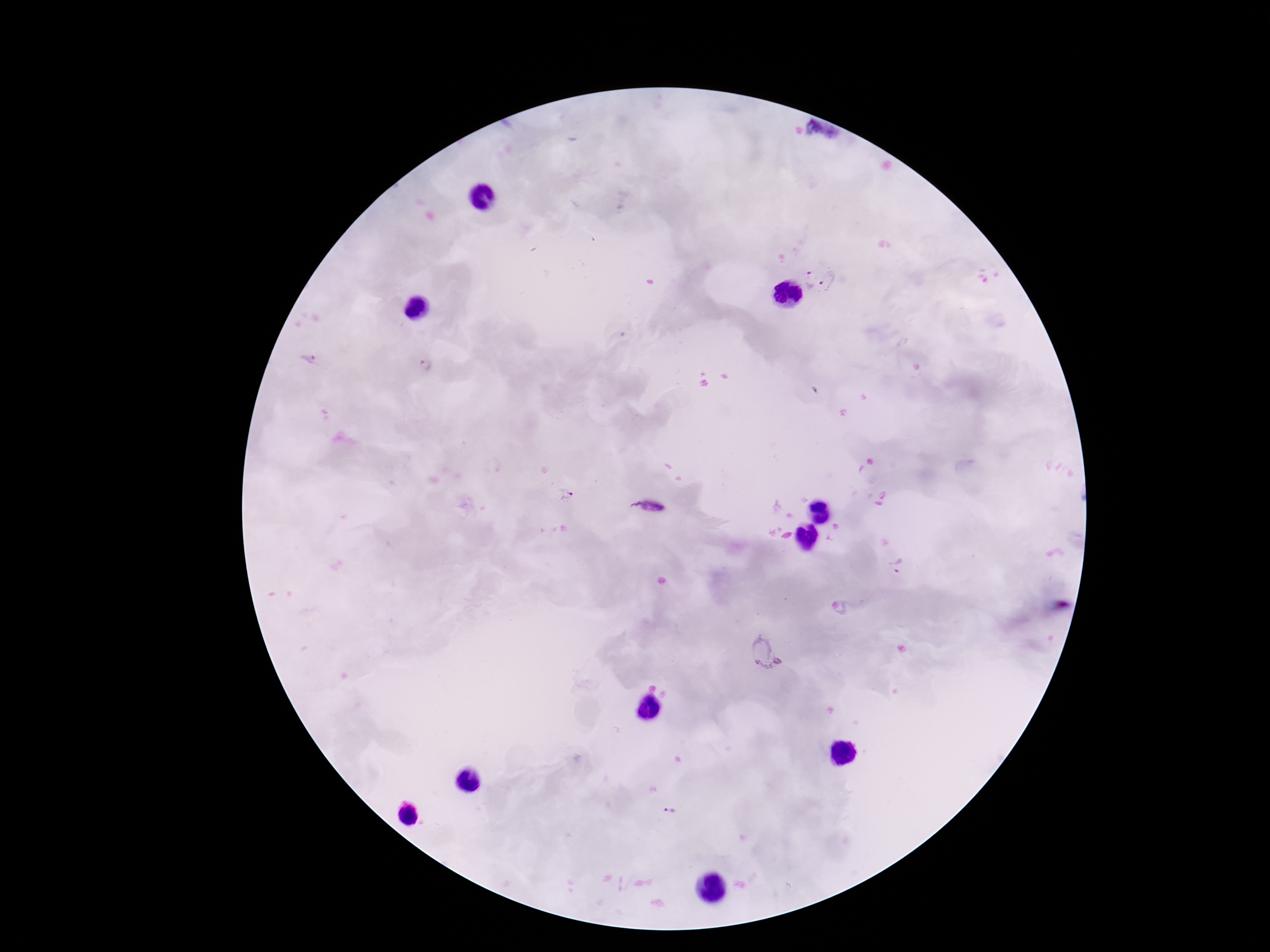

magnification = 100x
patient malaria status = positive
capture = smartphone camera through the microscope eyepiece
Plasmodium parasite locations = approximate centers as [x, y] in pixels: [806, 278], [832, 284], [423, 367], [565, 494], [649, 506], [895, 566], [769, 654], [670, 811]
preparation = thick blood film
image size = 1270×952 pixels
stain = Giemsa
field of view = single